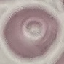

Summary:
  - Malaria status: uninfected
  - Image type: cell patch, automatically extracted from a larger field of view and resized to 64 × 64 pixels
  - Capture: smartphone through the microscope eyepiece
  - Stain: Giemsa
  - Preparation: thin blood smear